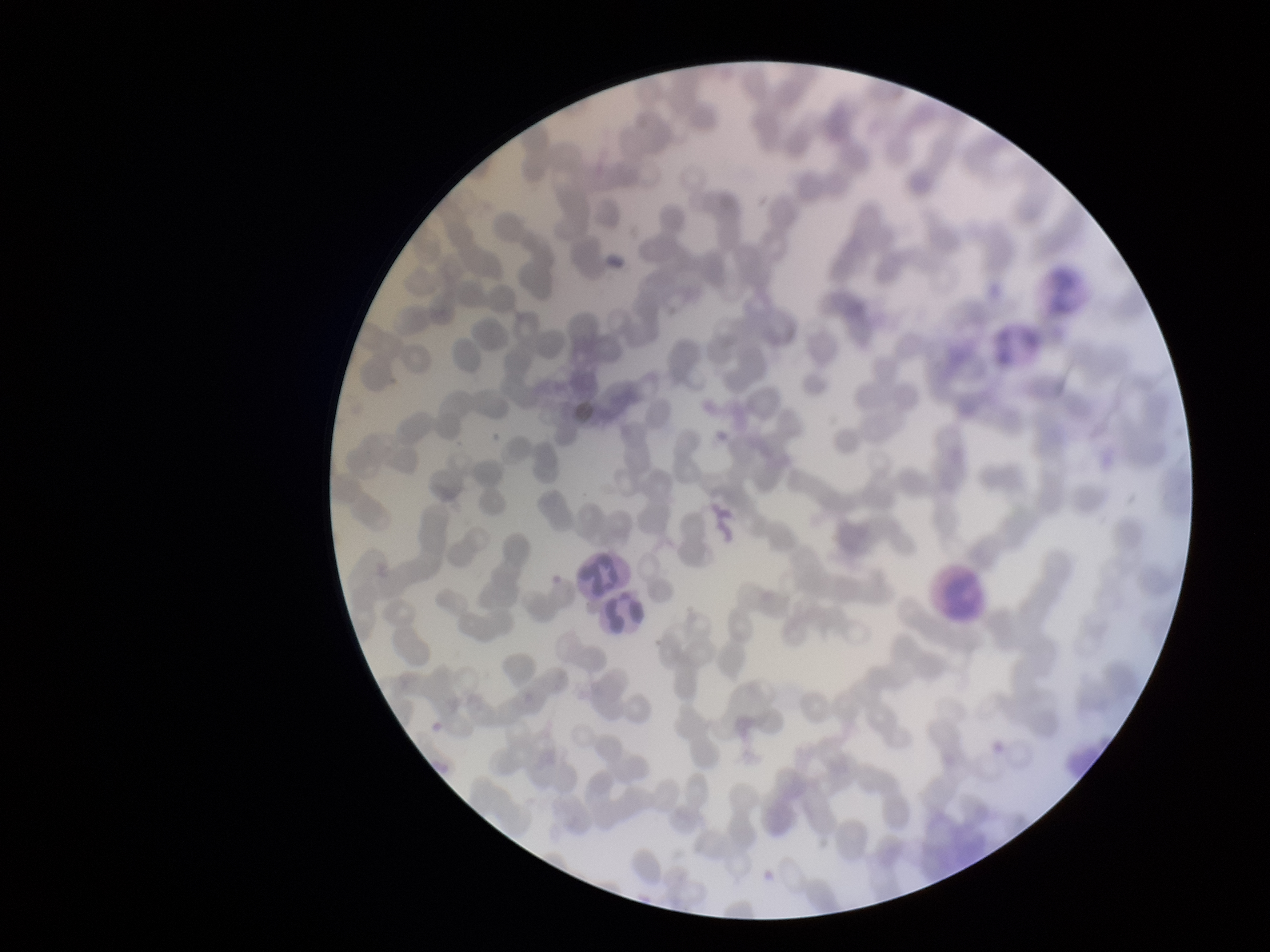

red blood cell count = 268
stain = Giemsa
patient malaria status = negative
field of view = single
preparation = thin
parasitized red blood cell count = 0
image size = 1270×952 pixels
capture = smartphone photograph through the microscope eyepiece
parasitized red blood cells = none seen